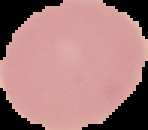 From a thin blood smear. Cell region segmented out of the field of view; the surrounding area is masked to black. Result: no Plasmodium parasites detected. Image is 148×130 pixels.